Locate every malaria parasite and every leukocyte.
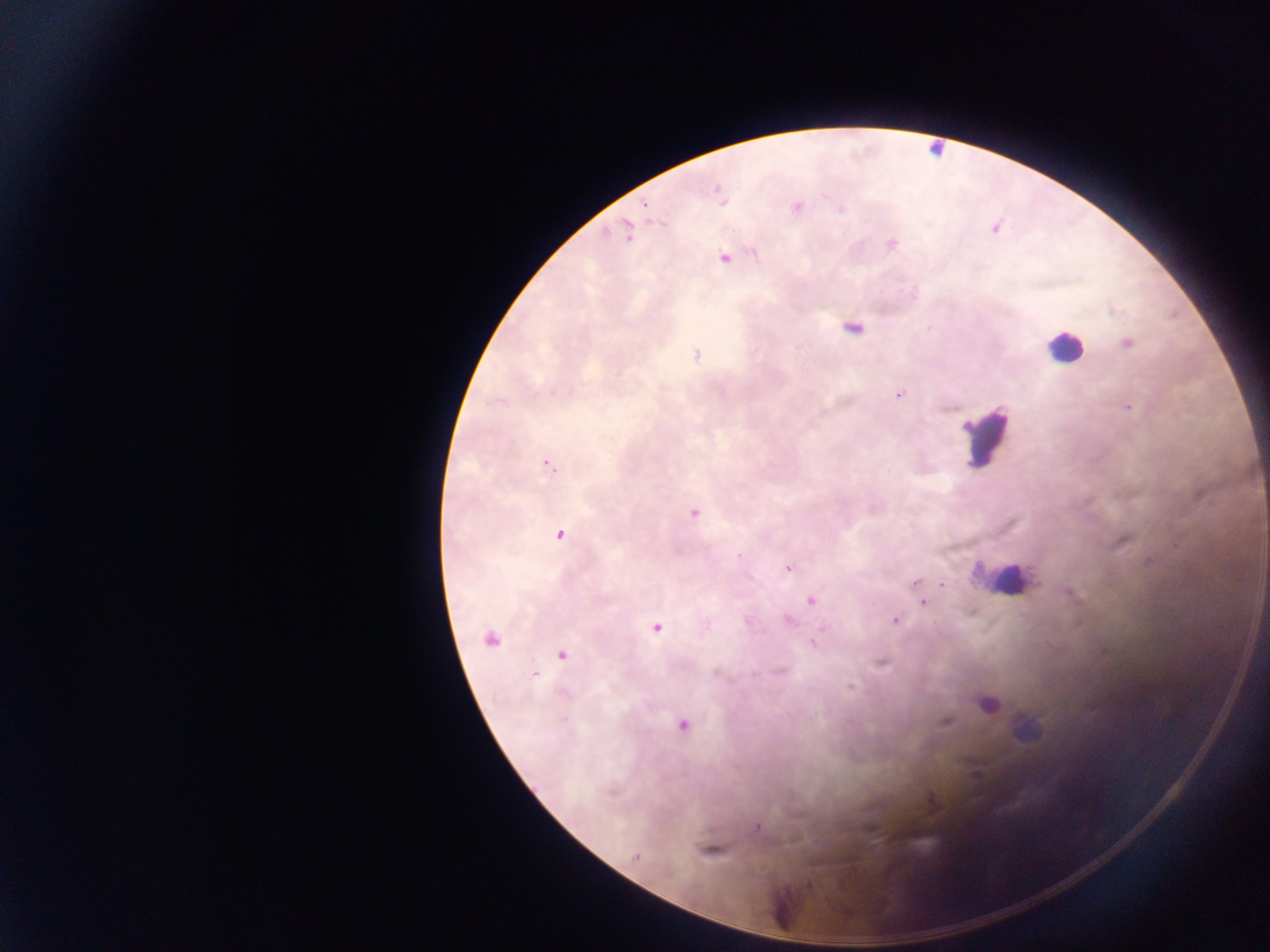
Approximate centers as {x, y} in pixels.
Malaria parasites: {719, 194}, {797, 208}, {995, 228}, {627, 234}, {892, 244}, {724, 259}, {852, 329}, {1127, 343}, {697, 354}, {900, 395}, {1128, 407}, {548, 465}, {693, 513}, {560, 534}, {1122, 543}, {739, 555}, {789, 568}, {916, 582}, {942, 584}, {811, 601}, {923, 602}, {790, 620}, {895, 621}, {657, 628}, {490, 638}, {815, 643}, {562, 655}, {533, 673}, {989, 703}, {945, 722}, {682, 725}, {757, 827}, {710, 850}, {636, 857}, {808, 886}.
Leukocytes: {1064, 346}, {986, 435}, {1006, 579}.

capture: mobile-phone photograph through a microscope
field_of_view: single
image_size: 1270×952 pixels
country: Ghana
preparation: thick blood film